Name the parasite shown.
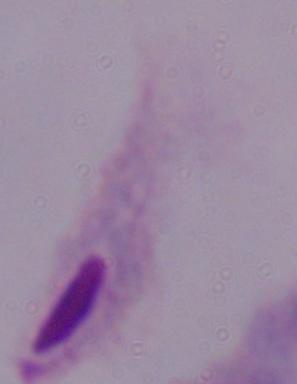

A trichomonad.

modality: micrograph
magnification: 1000x